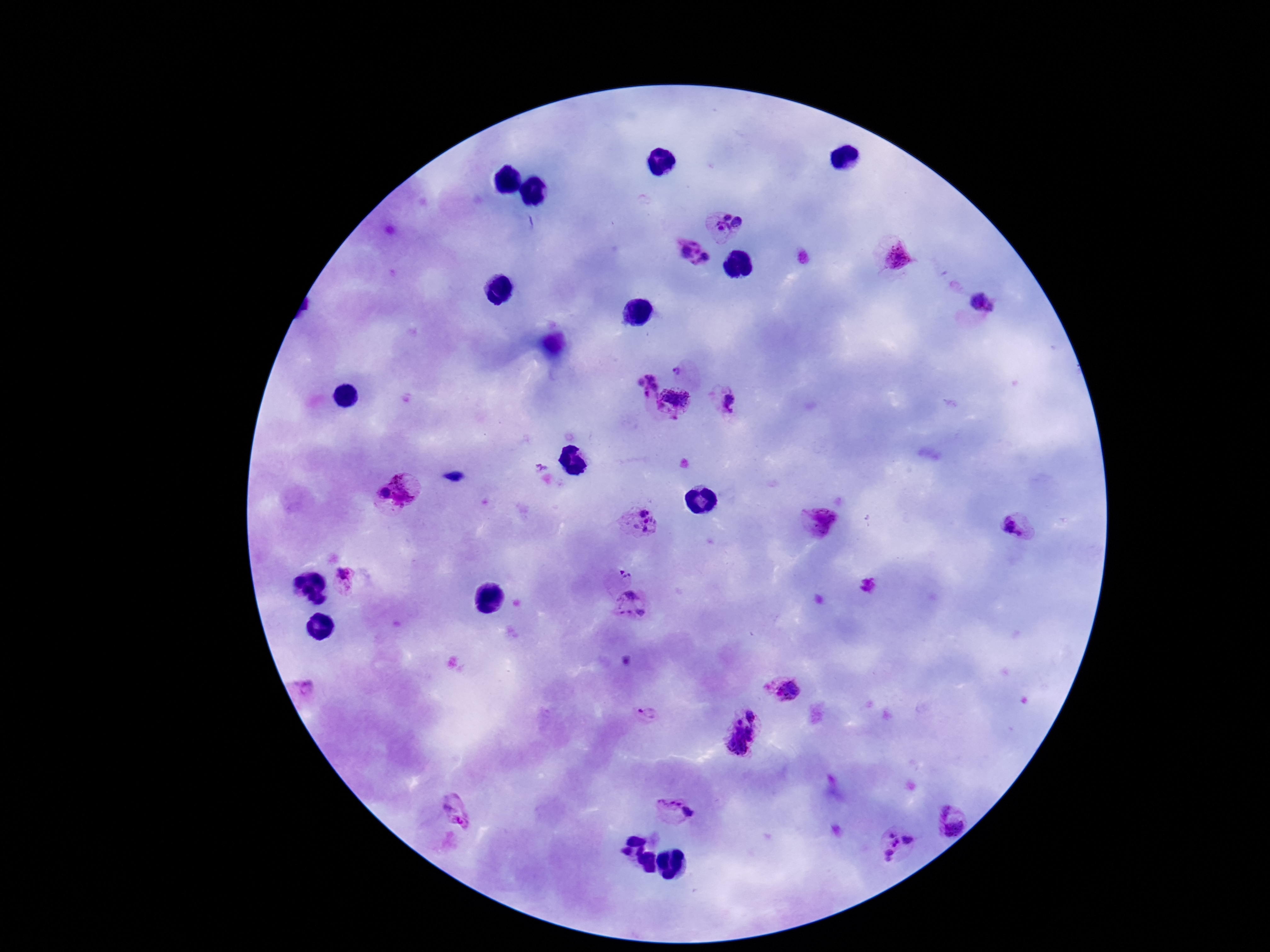 Approximate centers as (x, y) in pixels. Plasmodium parasite locations: (726, 226), (690, 252), (896, 259), (982, 303), (686, 372), (648, 383), (674, 401), (731, 406), (395, 495), (819, 518), (641, 522), (1014, 526), (623, 575), (348, 583), (629, 603), (307, 689), (786, 690), (647, 715), (744, 734), (674, 811), (457, 814), (954, 816), (901, 846). Thick blood film. Patient malaria status: positive. One field from this slide. Giemsa-stained preparation. Photographed through the microscope eyepiece with a smartphone camera. Image is 1270×952 pixels. 100x magnification.